Name the parasite shown.
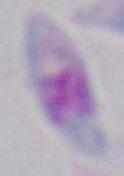
Toxoplasma gondii.

Summary:
  - Modality: micrograph
  - Magnification: 1000x